Comment on the morphology of the erythrocytes.
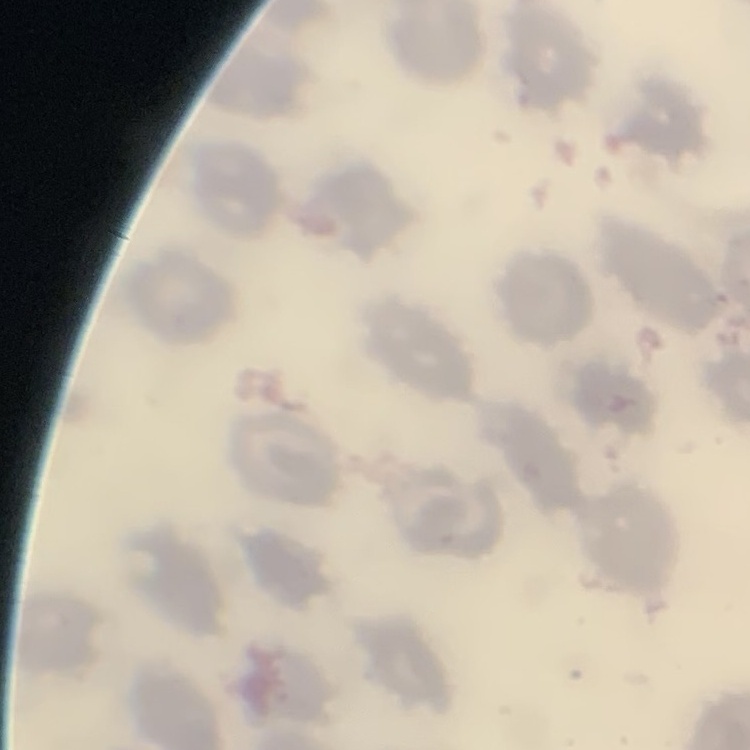

They show no rouleaux formation.

Field's or Giemsa stain. Square crop of a larger photomicrograph. Thin blood smear.